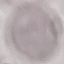

Result: no malaria parasites detected. Thin blood film. Photographed with a smartphone camera at the microscope eyepiece. Giemsa stain. Cell patch, automatically extracted from a larger field of view and resized to 64 × 64 pixels.